Give the preparation type.
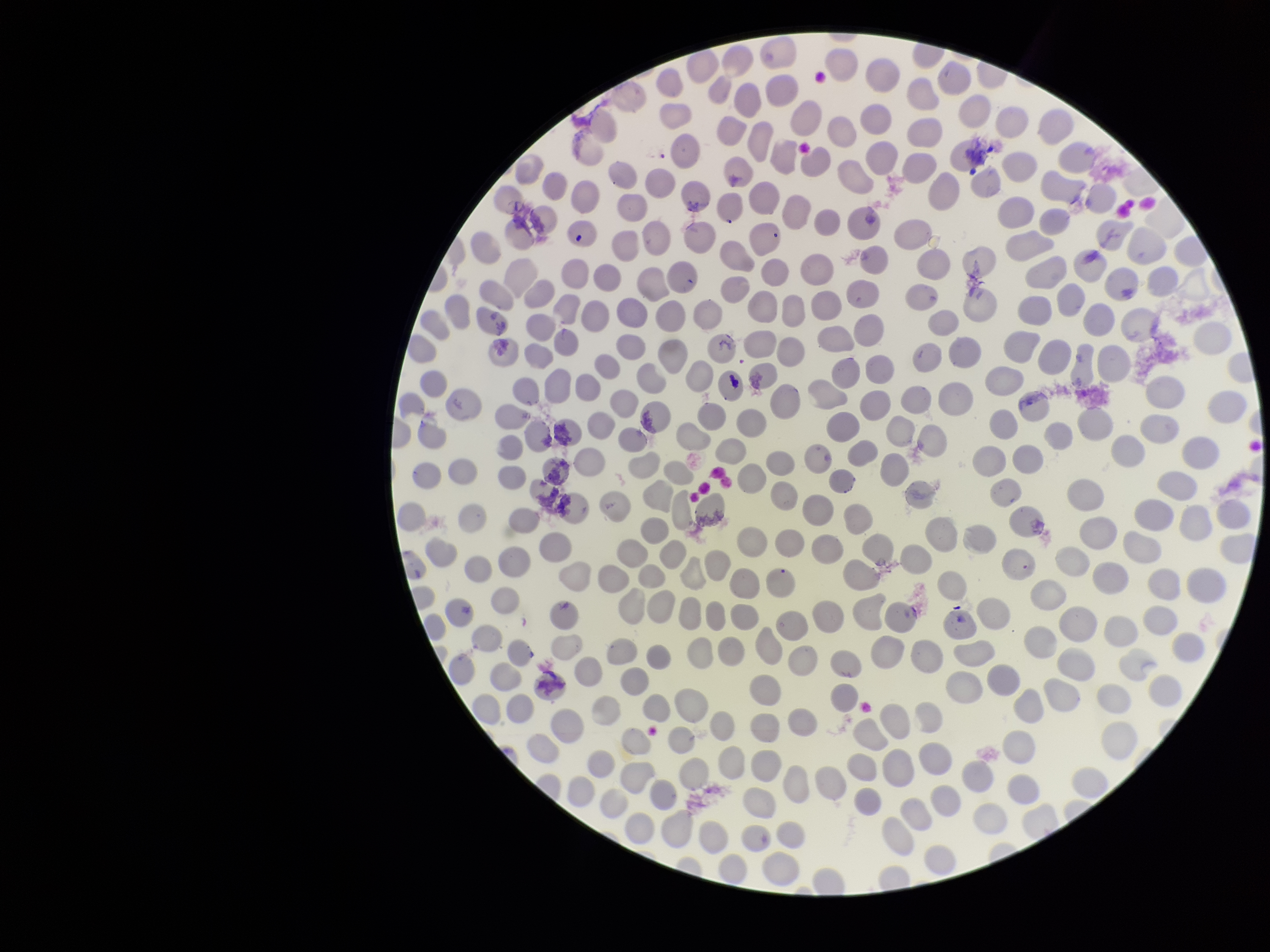

Thin.

Summary:
  - Image size: 1270×952 pixels
  - Stain: Giemsa
  - Field of view: single
  - Parasitized red blood cell count: 0
  - Capture: smartphone photograph through the microscope eyepiece
  - Parasitized red blood cells: none detected
  - Red blood cell count: 320
  - Patient malaria status: negative